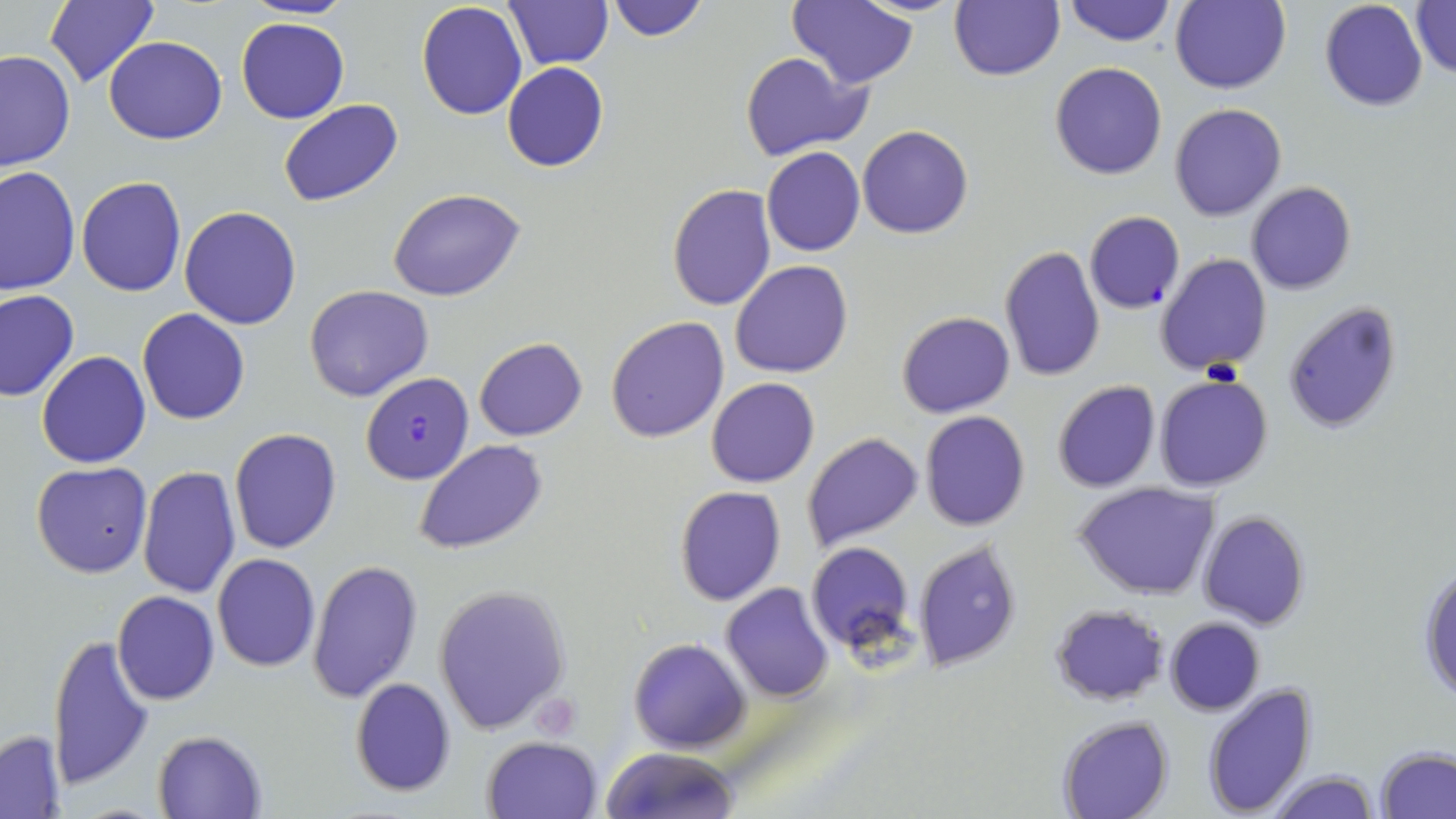

Approximate bounding boxes as [x1, y1, x2, y2] in pixels. Platelet locations: [530, 697, 581, 738]. Plasmodium falciparum-infected red blood cell locations: [361, 373, 474, 485]. Uninfected red blood cell locations: [45, 0, 160, 88], [244, 0, 354, 20], [503, 0, 611, 71], [606, 0, 709, 42], [950, 0, 1064, 81], [1171, 0, 1291, 95], [1409, 0, 1456, 79], [416, 1, 528, 121], [786, 1, 918, 88], [1063, 1, 1178, 47], [1318, 1, 1429, 113], [236, 16, 349, 123], [104, 35, 229, 144], [1, 49, 77, 172], [743, 51, 871, 160], [1050, 61, 1167, 180], [501, 62, 608, 172], [277, 100, 404, 206], [1169, 102, 1287, 220], [857, 125, 973, 239], [762, 147, 865, 256], [0, 164, 79, 295], [76, 175, 187, 296], [1246, 181, 1356, 294], [666, 184, 777, 312], [387, 186, 527, 303], [178, 205, 301, 330], [1084, 210, 1184, 313], [999, 246, 1106, 381], [1155, 252, 1273, 374], [731, 260, 854, 379], [304, 285, 435, 402], [0, 289, 79, 401], [1284, 301, 1402, 434], [137, 308, 250, 425], [897, 311, 1014, 418], [605, 315, 730, 444], [474, 337, 587, 442], [36, 350, 151, 468], [1153, 372, 1274, 493], [706, 377, 819, 488], [1052, 381, 1160, 493], [919, 411, 1030, 531], [228, 428, 342, 554], [802, 432, 922, 549], [414, 439, 551, 553], [141, 451, 330, 579], [31, 461, 153, 578], [136, 466, 240, 597], [1073, 482, 1218, 601], [675, 486, 787, 607], [1198, 509, 1311, 630], [912, 540, 1024, 673], [806, 541, 916, 659], [211, 554, 321, 672], [306, 560, 423, 703], [1418, 563, 1456, 704], [719, 583, 834, 701], [432, 584, 571, 734], [111, 590, 220, 706], [1048, 603, 1169, 707], [67, 604, 199, 757], [1165, 617, 1265, 715], [46, 632, 154, 789], [628, 638, 750, 754], [348, 677, 457, 799], [1199, 683, 1321, 818], [1055, 715, 1175, 819], [152, 730, 267, 819], [0, 731, 67, 815], [481, 735, 605, 819], [603, 748, 743, 819], [1377, 748, 1456, 818], [1263, 771, 1381, 819]. Slide-level diagnosis: Plasmodium falciparum. One field of a larger specimen. Thin blood smear. 1000x magnification. May-Grünwald-Giemsa-stained preparation. Image is 1456×819 pixels. Light microscopy.